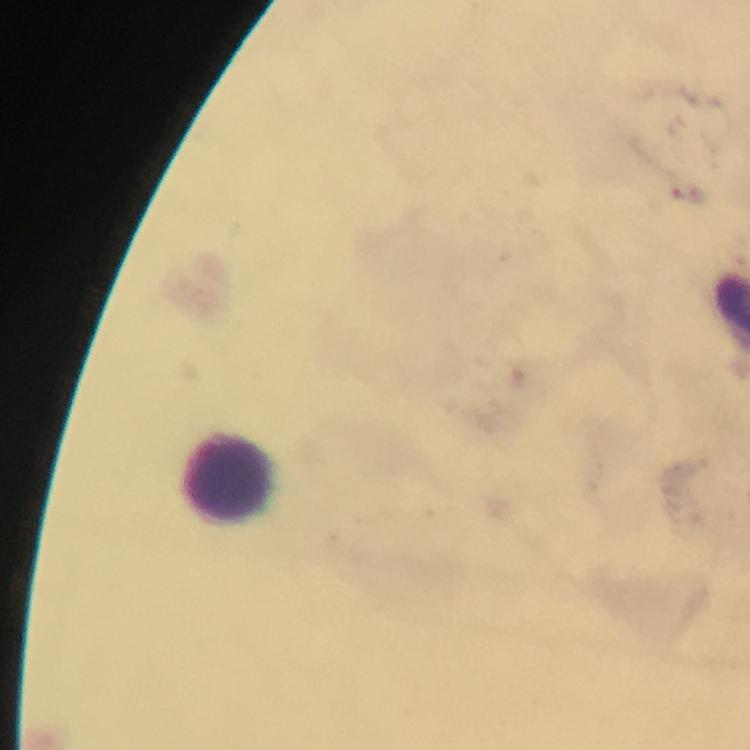

Approximate centers as {x, y} in pixels. Leukocyte locations: {229, 476}. Immersion oil applied. At 100x magnification. Giemsa-stained preparation. Malaria parasites: none detected. Photographed with a smartphone mounted on the microscope. A crop from one field of view. Thick blood smear. Image is 750×750 pixels. From a malaria diagnostic workup.